Locate every blood parasite and identify its species.
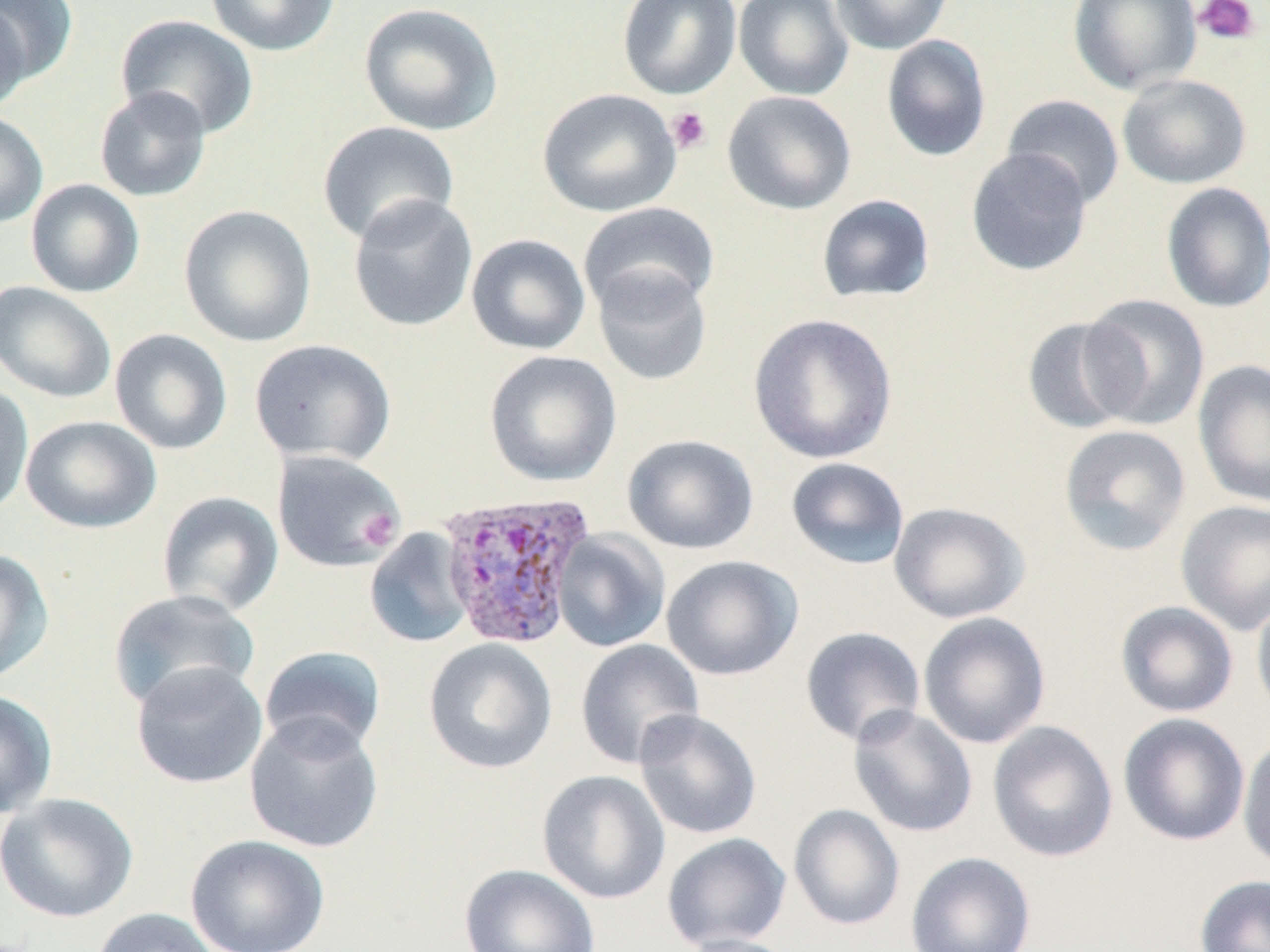

Approximate bounding boxes as [x1, y1, x2, y2] in pixels.
Plasmodium vivax-infected red blood cells: [437, 491, 596, 649].
No Plasmodium falciparum, Plasmodium ovale, Plasmodium malariae, Babesia divergens, or Trypanosoma brucei observed.

Summary:
  - Platelet locations: [1193, 0, 1260, 46], [666, 106, 713, 155], [359, 510, 401, 548]
  - Uninfected red blood cell locations: [0, 0, 78, 87], [205, 0, 340, 56], [616, 0, 742, 100], [733, 0, 853, 100], [829, 0, 954, 55], [1067, 0, 1202, 95], [358, 2, 503, 136], [0, 3, 31, 115], [115, 14, 259, 139], [881, 35, 991, 162], [1117, 73, 1252, 189], [94, 86, 212, 202], [537, 88, 681, 217], [722, 90, 856, 215], [1001, 94, 1125, 208], [0, 110, 48, 228], [317, 121, 460, 246], [965, 147, 1093, 276], [25, 179, 145, 298], [1161, 182, 1270, 313], [347, 194, 478, 332], [816, 194, 936, 303], [578, 201, 719, 317], [179, 204, 317, 347], [466, 234, 591, 355], [592, 266, 713, 386], [0, 282, 117, 403], [1079, 293, 1210, 430], [747, 312, 899, 464], [1021, 316, 1143, 435], [109, 328, 233, 455], [248, 338, 396, 466], [484, 350, 622, 487], [1192, 359, 1270, 508], [0, 381, 34, 518], [21, 415, 161, 533], [1058, 424, 1191, 556], [622, 434, 759, 555], [271, 450, 405, 573], [785, 457, 910, 570], [157, 491, 284, 617], [1176, 499, 1270, 636], [888, 501, 1030, 624], [364, 528, 476, 648], [552, 529, 671, 652], [0, 548, 54, 684], [661, 555, 803, 681], [108, 590, 261, 711], [1251, 591, 1270, 720], [1115, 601, 1239, 718], [918, 611, 1051, 749], [800, 626, 926, 747], [423, 638, 558, 774], [574, 639, 704, 769], [259, 645, 386, 757], [130, 660, 268, 789], [0, 689, 58, 819], [848, 706, 978, 838], [633, 708, 762, 840], [1118, 712, 1250, 846], [244, 713, 384, 853], [987, 720, 1118, 863], [1237, 733, 1270, 873], [537, 769, 670, 904], [1, 792, 139, 923], [788, 804, 905, 930], [662, 832, 792, 951], [186, 834, 331, 952], [905, 851, 1036, 952], [459, 863, 601, 952], [1195, 874, 1270, 952], [90, 907, 222, 952], [676, 933, 802, 952]
  - Slide-level diagnosis: Plasmodium vivax
  - Preparation: thin blood film
  - Magnification: 1000x
  - Stain: May-Grünwald-Giemsa
  - Field of view: one of a larger specimen
  - Image size: 1270×952 pixels
  - Modality: optical microscopy